Locate every Plasmodium falciparum-infected red blood cell.
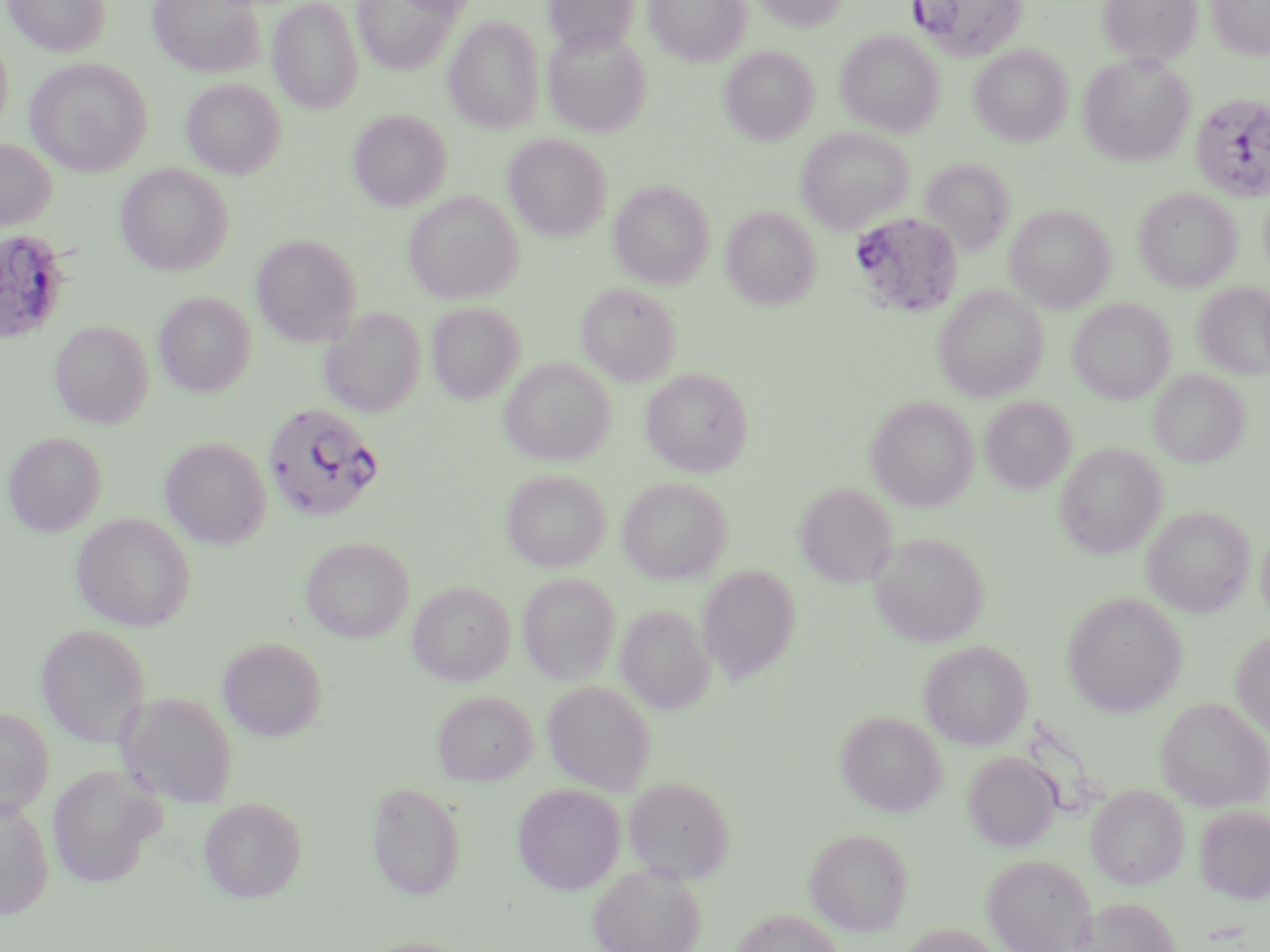
Approximate bounding boxes as named x1/y1/x2/y2 corners in pixels.
Plasmodium falciparum-infected red blood cells: (x1=910, y1=0, x2=1029, y2=61), (x1=1189, y1=92, x2=1270, y2=202), (x1=849, y1=213, x2=964, y2=319), (x1=0, y1=229, x2=73, y2=345), (x1=262, y1=401, x2=385, y2=522).

Summary:
  - Uninfected red blood cell locations: (x1=3, y1=0, x2=110, y2=57), (x1=148, y1=0, x2=265, y2=78), (x1=353, y1=0, x2=459, y2=75), (x1=392, y1=0, x2=485, y2=17), (x1=546, y1=0, x2=638, y2=55), (x1=644, y1=0, x2=753, y2=66), (x1=751, y1=0, x2=851, y2=31), (x1=1097, y1=0, x2=1203, y2=64), (x1=1207, y1=0, x2=1270, y2=59), (x1=268, y1=1, x2=363, y2=114), (x1=445, y1=17, x2=545, y2=134), (x1=543, y1=27, x2=653, y2=137), (x1=835, y1=30, x2=944, y2=137), (x1=0, y1=34, x2=14, y2=137), (x1=970, y1=45, x2=1073, y2=146), (x1=720, y1=46, x2=818, y2=145), (x1=1078, y1=54, x2=1195, y2=166), (x1=25, y1=57, x2=153, y2=177), (x1=181, y1=78, x2=286, y2=179), (x1=349, y1=110, x2=452, y2=211), (x1=795, y1=127, x2=914, y2=233), (x1=504, y1=135, x2=611, y2=240), (x1=0, y1=139, x2=56, y2=232), (x1=919, y1=157, x2=1016, y2=259), (x1=115, y1=164, x2=234, y2=275), (x1=609, y1=181, x2=715, y2=289), (x1=1134, y1=187, x2=1241, y2=291), (x1=404, y1=191, x2=523, y2=304), (x1=1005, y1=204, x2=1115, y2=312), (x1=722, y1=206, x2=821, y2=310), (x1=251, y1=234, x2=362, y2=346), (x1=1194, y1=282, x2=1270, y2=380), (x1=577, y1=283, x2=681, y2=385), (x1=933, y1=285, x2=1048, y2=402), (x1=153, y1=292, x2=256, y2=397), (x1=1068, y1=298, x2=1176, y2=404), (x1=427, y1=303, x2=524, y2=404), (x1=319, y1=308, x2=426, y2=417), (x1=50, y1=321, x2=154, y2=429), (x1=500, y1=357, x2=616, y2=466), (x1=640, y1=367, x2=754, y2=477), (x1=1149, y1=369, x2=1250, y2=467), (x1=865, y1=396, x2=979, y2=511), (x1=980, y1=396, x2=1076, y2=494), (x1=3, y1=432, x2=107, y2=536), (x1=160, y1=437, x2=272, y2=549), (x1=1054, y1=442, x2=1167, y2=559), (x1=501, y1=469, x2=611, y2=572), (x1=618, y1=476, x2=733, y2=583), (x1=795, y1=483, x2=897, y2=588), (x1=1143, y1=505, x2=1255, y2=617), (x1=71, y1=512, x2=196, y2=631), (x1=1257, y1=523, x2=1270, y2=628), (x1=869, y1=531, x2=989, y2=647), (x1=301, y1=537, x2=414, y2=643), (x1=696, y1=565, x2=801, y2=684), (x1=518, y1=573, x2=621, y2=685), (x1=408, y1=581, x2=516, y2=685), (x1=1062, y1=591, x2=1186, y2=716), (x1=617, y1=604, x2=714, y2=714), (x1=36, y1=624, x2=151, y2=748), (x1=1231, y1=629, x2=1270, y2=738), (x1=217, y1=637, x2=327, y2=741), (x1=919, y1=639, x2=1033, y2=749), (x1=542, y1=680, x2=656, y2=795), (x1=116, y1=691, x2=239, y2=807), (x1=432, y1=691, x2=538, y2=784), (x1=1156, y1=697, x2=1270, y2=811), (x1=0, y1=708, x2=54, y2=817), (x1=835, y1=709, x2=947, y2=816), (x1=963, y1=751, x2=1061, y2=851), (x1=47, y1=765, x2=165, y2=889), (x1=623, y1=774, x2=735, y2=882), (x1=366, y1=781, x2=467, y2=901), (x1=512, y1=783, x2=626, y2=895), (x1=1086, y1=784, x2=1189, y2=889), (x1=0, y1=795, x2=55, y2=918), (x1=198, y1=796, x2=308, y2=903), (x1=1195, y1=805, x2=1270, y2=903), (x1=805, y1=827, x2=914, y2=934), (x1=982, y1=852, x2=1095, y2=952), (x1=588, y1=862, x2=706, y2=952), (x1=1075, y1=897, x2=1182, y2=952), (x1=731, y1=908, x2=845, y2=952), (x1=897, y1=923, x2=1006, y2=952), (x1=356, y1=936, x2=471, y2=952)
  - Slide-level diagnosis: Plasmodium falciparum
  - Modality: optical microscopy
  - Image size: 1270×952 pixels
  - Preparation: thin blood smear
  - Magnification: 1000x
  - Field of view: single
  - Stain: May-Grünwald-Giemsa